Report the malaria status of this cell.
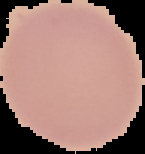
Uninfected.

preparation = thin blood smear
image type = segmented cell region with the area outside set to black
image size = 145×154 pixels